Classify this cell by malaria status.
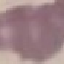

It is uninfected.

capture = smartphone through the microscope eyepiece
preparation = thin blood film
stain = Giemsa
image type = cell patch, automatically extracted from a larger field of view and resized to 64 × 64 pixels